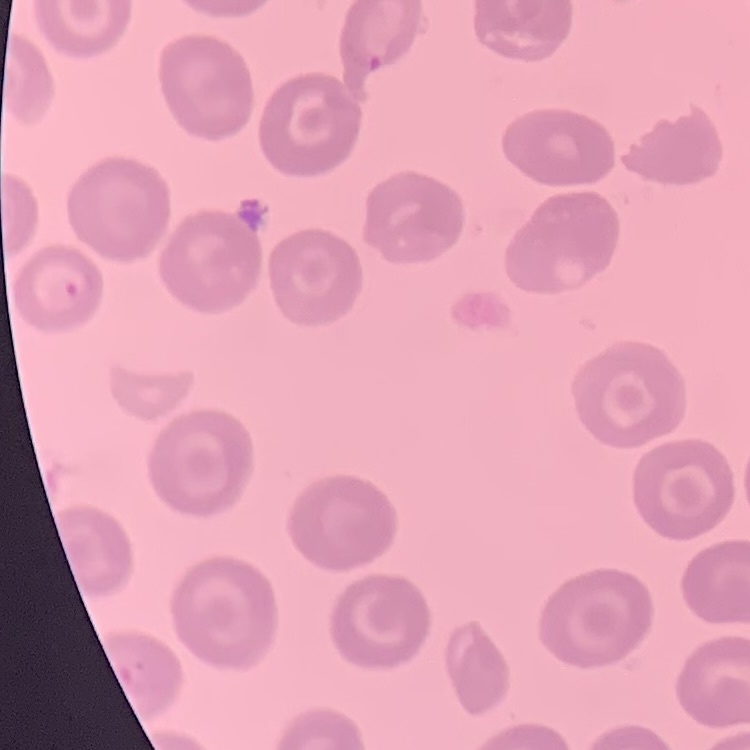
erythrocyte morphology = no rouleaux formation
image type = one tile cut from a larger photomicrograph
stain = Field's or Giemsa
preparation = thin peripheral smear